Classify this cell by malaria status.
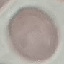

It is uninfected.

stain = Giemsa
image type = cell patch, automatically extracted from a larger field of view and resized to 64 × 64 pixels
preparation = thin blood smear
capture = smartphone through the microscope eyepiece